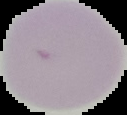
image type = cell region segmented out of the field of view; surrounding area masked to black
image size = 127×115 pixels
preparation = thin blood smear
malaria status = uninfected